Evaluate for parasitized red blood cells.
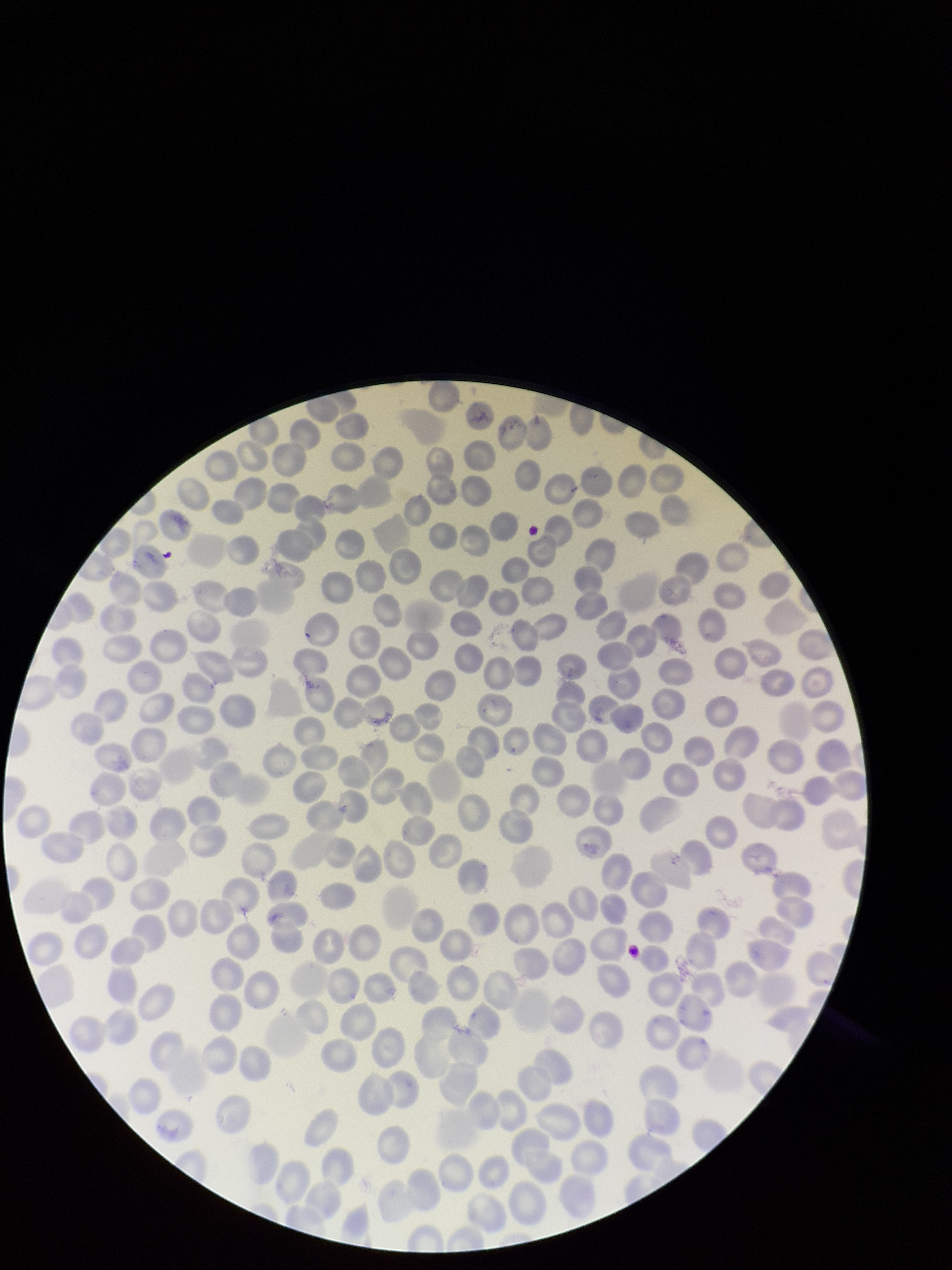

None seen.

Giemsa stain. Species reported for this patient: Plasmodium falciparum. Image is 952×1270 pixels. Red blood cell count: 242. Preparation: thin blood smear. Patient malaria status: infected. Photographed through the microscope eyepiece with a smartphone camera. Parasitized red blood cell count: 0. Single field of view.